Locate and identify every blood parasite.
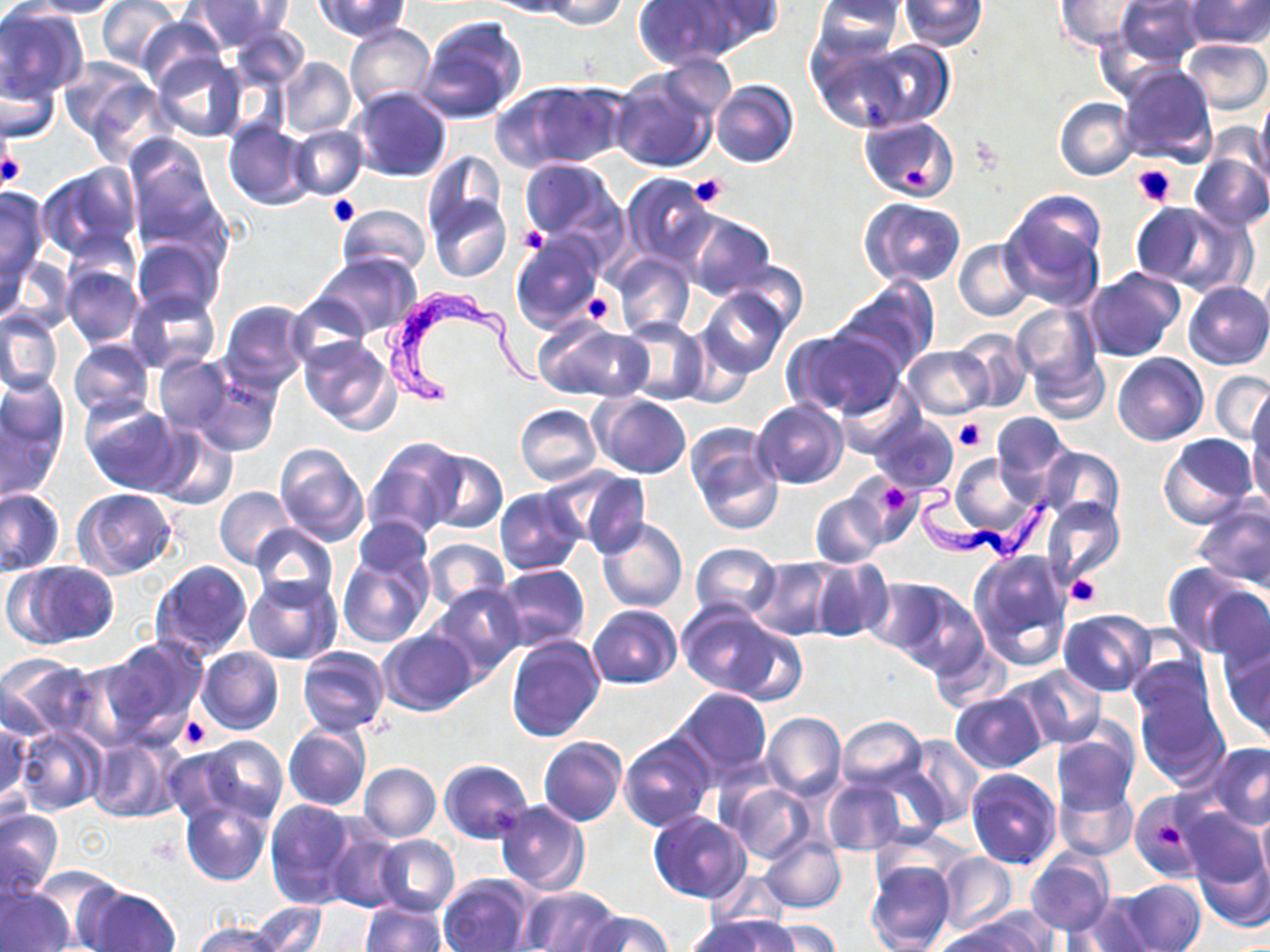

Approximate bounding boxes as (x1, y1, x2, y2) in pixels.
Trypanosoma brucei: (382, 282, 541, 407), (909, 475, 1047, 565).
No Plasmodium falciparum, Plasmodium ovale, Plasmodium malariae, Plasmodium vivax, or Babesia divergens observed.

slide-level diagnosis = Trypanosoma brucei
image size = 1270×952 pixels
field of view = single
modality = optical microscopy
uninfected red blood cell locations = approximate bounding boxes as (x1, y1, x2, y2) in pixels: (20, 0, 123, 18), (97, 0, 182, 71), (192, 0, 292, 49), (317, 0, 410, 41), (483, 0, 577, 17), (539, 0, 629, 29), (632, 0, 736, 68), (691, 0, 784, 49), (812, 0, 903, 65), (900, 0, 987, 50), (1114, 0, 1203, 66), (1187, 0, 1270, 50), (1055, 1, 1142, 52), (0, 5, 87, 104), (136, 14, 224, 91), (413, 14, 527, 127), (231, 22, 308, 91), (344, 22, 435, 112), (807, 38, 910, 130), (1183, 38, 1269, 115), (857, 41, 953, 129), (151, 54, 248, 143), (656, 55, 736, 120), (278, 57, 356, 138), (64, 60, 164, 157), (1, 62, 61, 143), (1116, 65, 1218, 166), (610, 70, 720, 174), (709, 79, 798, 169), (500, 81, 626, 170), (347, 87, 454, 182), (1255, 93, 1270, 181), (1055, 97, 1139, 181), (858, 116, 960, 202), (223, 120, 314, 209), (288, 126, 367, 200), (122, 136, 224, 253), (421, 151, 506, 242), (1189, 153, 1270, 232), (518, 158, 620, 244), (37, 163, 142, 262), (621, 174, 720, 268), (0, 187, 51, 288), (426, 193, 511, 284), (999, 195, 1106, 309), (861, 199, 967, 288), (1133, 202, 1236, 291), (337, 203, 431, 277), (682, 211, 777, 300), (511, 234, 605, 334), (132, 237, 224, 320), (955, 240, 1035, 322), (614, 252, 694, 339), (314, 253, 421, 337), (3, 255, 76, 335), (727, 263, 808, 337), (61, 265, 143, 347), (1083, 268, 1184, 362), (828, 279, 937, 380), (1183, 281, 1270, 369), (696, 287, 789, 379), (127, 289, 221, 374), (287, 296, 372, 367), (218, 300, 311, 390), (1009, 303, 1103, 398), (0, 310, 62, 397), (619, 317, 708, 405), (536, 319, 653, 403), (785, 329, 906, 419), (953, 330, 1033, 413), (297, 336, 400, 435), (68, 338, 154, 420), (902, 346, 994, 418), (1027, 351, 1110, 425), (1113, 352, 1209, 446), (153, 355, 231, 433), (192, 368, 281, 457), (1211, 370, 1270, 444), (0, 380, 69, 496), (834, 381, 924, 458), (592, 394, 692, 479), (753, 399, 849, 489), (1246, 399, 1270, 506), (80, 400, 187, 495), (515, 404, 602, 485), (990, 411, 1070, 491), (871, 415, 958, 496), (684, 422, 783, 534), (149, 427, 236, 511), (1159, 434, 1260, 530), (364, 437, 465, 540), (274, 444, 368, 546), (1038, 446, 1125, 528), (424, 451, 507, 534), (947, 453, 1041, 543), (564, 469, 652, 559), (848, 473, 924, 550), (214, 486, 294, 570), (0, 488, 66, 576), (72, 488, 176, 579), (494, 488, 587, 576), (810, 491, 887, 568), (1043, 498, 1126, 586), (1193, 500, 1270, 592), (355, 515, 431, 585), (597, 519, 688, 613), (249, 524, 337, 608), (422, 538, 510, 613), (337, 542, 433, 647), (690, 542, 781, 621), (969, 550, 1072, 669), (749, 558, 839, 640), (809, 558, 891, 642), (7, 561, 120, 647), (149, 561, 253, 660), (497, 564, 590, 653), (1186, 574, 1270, 666), (244, 575, 342, 664), (863, 575, 958, 662), (429, 583, 525, 679), (892, 584, 991, 680), (589, 604, 681, 688), (677, 605, 790, 697), (1058, 610, 1156, 696), (726, 626, 808, 706), (378, 630, 477, 716), (927, 633, 1010, 715), (506, 634, 606, 741), (99, 637, 208, 744), (197, 647, 284, 735), (296, 647, 390, 736), (1221, 648, 1270, 744), (0, 654, 97, 741), (67, 658, 160, 751), (1015, 665, 1107, 749), (1133, 680, 1231, 788), (672, 687, 773, 780), (950, 691, 1048, 772), (762, 712, 846, 799), (836, 715, 926, 793), (0, 718, 31, 813), (283, 723, 371, 812), (14, 725, 105, 816), (1050, 726, 1140, 818), (618, 732, 716, 833), (902, 734, 985, 828), (183, 736, 289, 827), (87, 737, 178, 822), (539, 737, 627, 827), (1205, 743, 1270, 831), (440, 759, 532, 843), (824, 762, 981, 849), (360, 763, 440, 841), (965, 769, 1060, 869), (820, 778, 908, 857), (1052, 779, 1138, 861), (722, 781, 815, 863), (1129, 793, 1209, 882), (180, 795, 271, 886), (265, 798, 358, 907), (495, 801, 590, 894), (0, 808, 64, 898), (1179, 808, 1269, 891), (1256, 809, 1270, 893), (648, 810, 751, 903), (323, 823, 406, 913), (374, 835, 460, 916), (760, 837, 845, 913), (1191, 837, 1270, 934), (936, 852, 1017, 934), (1025, 852, 1114, 934), (865, 859, 955, 952), (26, 867, 122, 947), (440, 876, 534, 952), (1118, 878, 1205, 952), (0, 885, 75, 952), (517, 885, 619, 952), (79, 886, 181, 952), (1063, 897, 1156, 951), (361, 901, 446, 952), (247, 902, 327, 952), (581, 911, 674, 952), (953, 912, 1054, 952), (690, 917, 792, 952), (759, 919, 841, 952), (192, 920, 282, 952), (930, 926, 1033, 952)
platelet locations = approximate bounding boxes as (x1, y1, x2, y2) in pixels: (0, 145, 23, 192), (1131, 164, 1177, 208), (900, 168, 929, 189), (689, 173, 728, 209), (328, 194, 359, 225), (519, 227, 548, 254), (581, 291, 616, 324), (953, 416, 988, 452), (882, 480, 919, 512), (1067, 573, 1101, 608), (179, 715, 212, 750), (1155, 819, 1184, 850)
magnification = 1000x
stain = May-Grünwald-Giemsa
preparation = thin blood smear